Identify the blood parasite species.
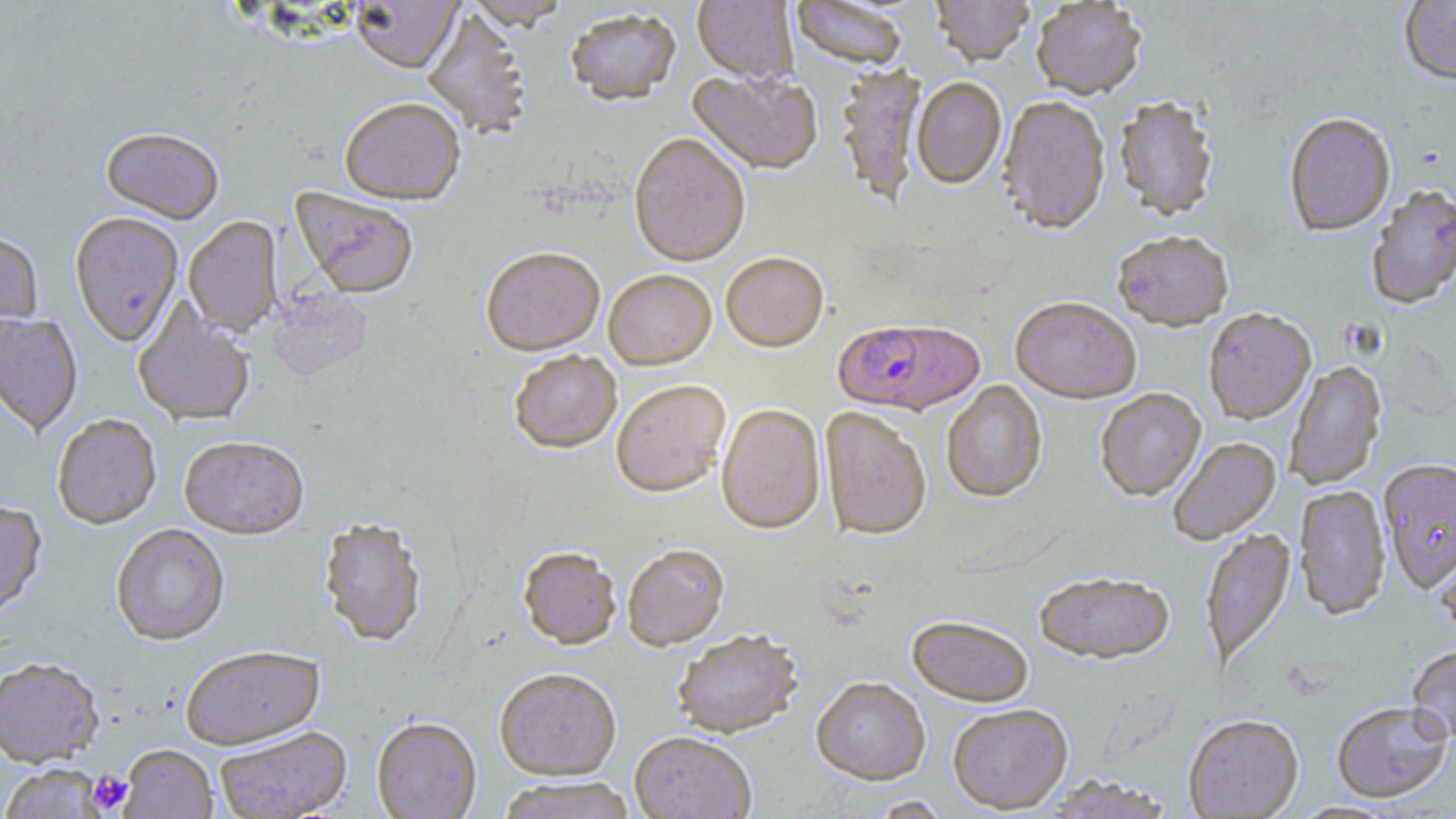

Plasmodium falciparum.

Summary:
  - Coordinate format: approximate bounding boxes as [x1, y1, x2, y2] in pixels
  - Uninfected red blood cell locations: [466, 0, 571, 33], [692, 0, 798, 86], [930, 0, 1034, 69], [1399, 0, 1456, 88], [349, 1, 463, 77], [1031, 1, 1146, 103], [791, 2, 908, 72], [422, 9, 531, 140], [566, 11, 682, 109], [835, 67, 927, 208], [686, 71, 823, 177], [911, 79, 1007, 191], [1113, 98, 1218, 224], [997, 99, 1111, 238], [339, 100, 465, 208], [1283, 115, 1396, 239], [100, 129, 224, 225], [628, 135, 750, 271], [1366, 187, 1456, 312], [289, 188, 418, 301], [69, 214, 184, 348], [184, 218, 283, 337], [0, 231, 43, 339], [1113, 233, 1233, 335], [481, 250, 605, 359], [720, 254, 828, 355], [603, 272, 717, 372], [266, 289, 371, 382], [1010, 299, 1141, 407], [132, 300, 255, 428], [1204, 310, 1316, 426], [1, 313, 83, 437], [509, 352, 622, 455], [1285, 360, 1388, 491], [941, 381, 1047, 505], [611, 383, 731, 500], [1095, 389, 1207, 503], [716, 405, 826, 536], [820, 409, 930, 543], [52, 417, 161, 532], [1168, 438, 1282, 546], [179, 439, 309, 541], [1378, 461, 1456, 595], [1293, 486, 1391, 622], [0, 501, 48, 623], [318, 520, 427, 649], [112, 525, 229, 648], [1200, 529, 1297, 670], [1434, 544, 1456, 647], [623, 546, 730, 652], [517, 549, 621, 652], [1035, 576, 1175, 667], [906, 618, 1034, 709], [672, 631, 803, 741], [1406, 645, 1456, 746], [181, 647, 326, 753], [0, 661, 104, 770], [494, 671, 621, 782], [812, 679, 931, 788], [1331, 704, 1453, 805], [948, 705, 1073, 815], [1184, 717, 1303, 818], [371, 719, 482, 819], [215, 728, 353, 819], [630, 733, 756, 819], [118, 746, 217, 819], [1, 766, 108, 819], [1043, 776, 1174, 819], [495, 778, 638, 819]
  - Platelet locations: [88, 770, 133, 814]
  - Plasmodium falciparum-infected red blood cell locations: [834, 322, 984, 419]
  - Modality: light microscopy
  - Stain: May-Grünwald-Giemsa
  - Image size: 1456×819 pixels
  - Field of view: single
  - Preparation: thin blood smear
  - Magnification: 1000x